Assess this cell for malaria.
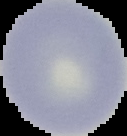
It is uninfected.

Summary:
  - Image type: cell region segmented out of the field of view; surrounding area masked to black
  - Preparation: thin blood smear
  - Image size: 127×136 pixels